Point out each Plasmodium parasite.
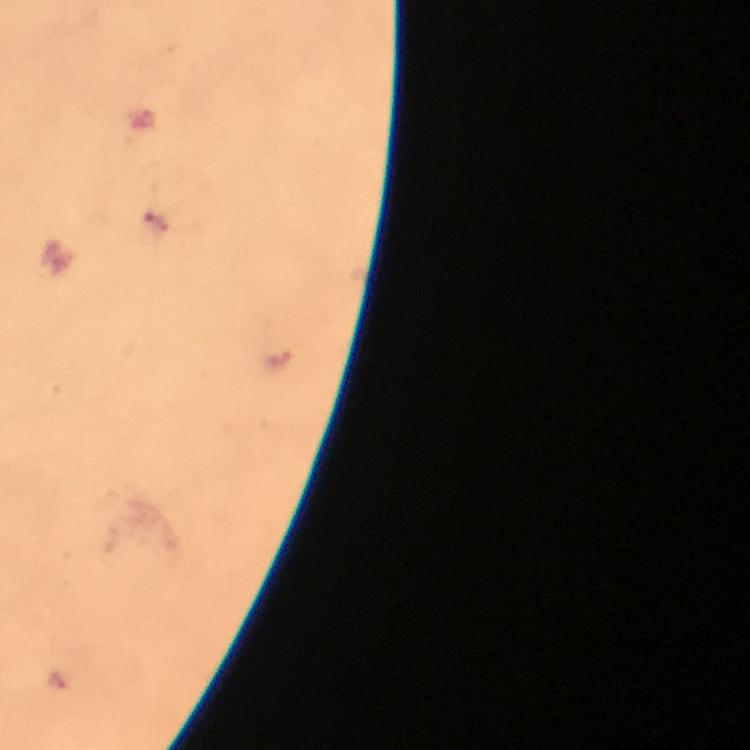
Approximate centers as [x, y] in pixels.
Plasmodium parasites: [59, 681].

Summary:
  - Context: from a diagnostic examination for malaria
  - Immersion oil: used
  - Magnification: 100x
  - Image size: 750×750 pixels
  - Capture: smartphone mounted on the microscope
  - Cropped from: a single field of view
  - Stain: Giemsa
  - Preparation: thick blood smear